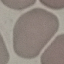

malaria status = uninfected
image type = cell patch, automatically extracted from a larger field of view and resized to 64 × 64 pixels
preparation = thin blood film
capture = smartphone through the microscope eyepiece
stain = Giemsa